Locate and identify every blood parasite.
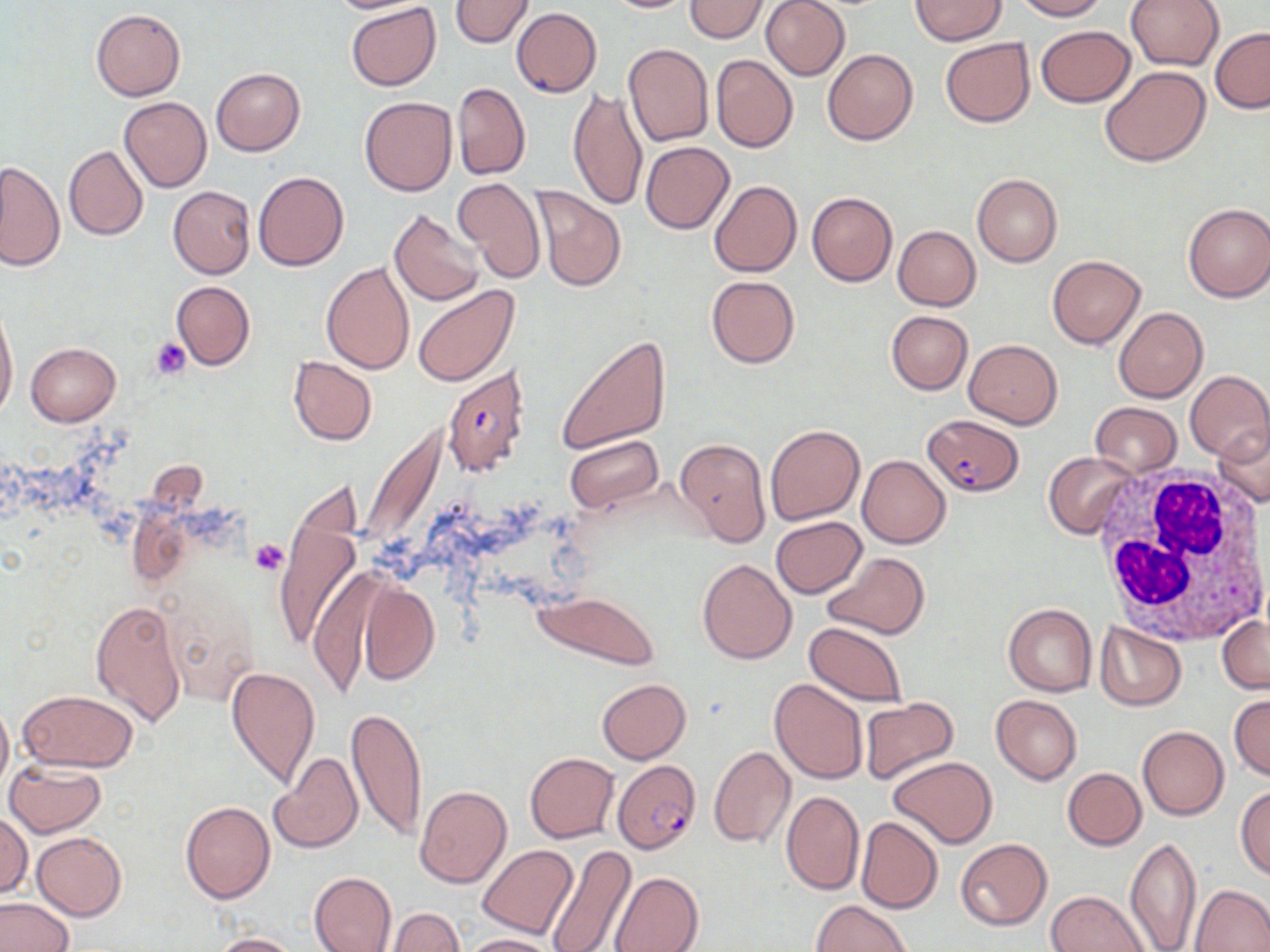

Approximate bounding boxes as [x1, y1, x2, y2] in pixels.
Plasmodium falciparum-infected red blood cells: [442, 367, 531, 476], [923, 414, 1024, 496], [613, 759, 700, 854].
No Plasmodium ovale, Plasmodium malariae, Plasmodium vivax, Babesia divergens, or Trypanosoma brucei observed.

Uninfected red blood cell locations: [324, 0, 431, 14], [449, 0, 535, 49], [603, 0, 700, 14], [687, 0, 769, 42], [760, 0, 849, 80], [910, 0, 1009, 44], [1010, 0, 1106, 21], [1124, 0, 1223, 71], [346, 3, 441, 91], [512, 7, 602, 97], [91, 9, 185, 101], [1035, 25, 1135, 107], [1210, 27, 1270, 113], [940, 38, 1034, 127], [623, 44, 713, 147], [822, 49, 917, 145], [711, 54, 797, 152], [211, 66, 305, 154], [1100, 66, 1208, 167], [452, 82, 530, 179], [568, 88, 648, 213], [118, 97, 210, 192], [359, 97, 457, 196], [640, 142, 734, 234], [64, 145, 147, 242], [0, 159, 65, 271], [253, 172, 348, 271], [971, 174, 1062, 267], [453, 178, 545, 281], [709, 178, 802, 278], [168, 185, 255, 278], [531, 186, 626, 291], [807, 192, 897, 287], [1182, 203, 1270, 302], [389, 209, 483, 307], [893, 225, 980, 311], [1047, 255, 1145, 348], [321, 262, 415, 374], [706, 275, 800, 367], [170, 280, 254, 370], [413, 284, 520, 389], [0, 304, 18, 425], [1114, 307, 1208, 402], [886, 311, 973, 394], [556, 334, 672, 455], [963, 339, 1063, 428], [26, 343, 120, 425], [287, 357, 378, 445], [1185, 370, 1270, 462], [1091, 403, 1182, 477], [358, 424, 446, 552], [765, 425, 864, 525], [1213, 425, 1269, 508], [564, 435, 664, 516], [674, 438, 771, 549], [1044, 452, 1136, 539], [856, 455, 950, 548], [276, 483, 361, 649], [771, 516, 867, 598], [822, 551, 928, 640], [696, 557, 797, 663], [309, 568, 382, 703], [358, 579, 440, 684], [532, 589, 660, 672], [164, 592, 259, 703], [90, 599, 188, 730], [1003, 603, 1097, 696], [1217, 615, 1269, 694], [1095, 621, 1185, 711], [804, 622, 907, 706], [225, 666, 321, 788], [596, 678, 691, 764], [769, 678, 869, 786], [18, 689, 139, 772], [1229, 693, 1270, 781], [990, 694, 1082, 784], [0, 695, 13, 794], [858, 696, 960, 787], [346, 707, 429, 839], [1137, 726, 1229, 820], [708, 747, 796, 850], [270, 752, 363, 854], [525, 753, 619, 842], [887, 755, 997, 848], [4, 762, 106, 837], [1063, 767, 1146, 850], [415, 785, 512, 889], [1235, 785, 1270, 880], [781, 791, 864, 895], [180, 801, 275, 904], [0, 813, 32, 897], [855, 816, 942, 914], [32, 831, 126, 921], [1125, 836, 1200, 952], [955, 838, 1052, 930], [477, 844, 577, 940], [545, 844, 638, 952], [309, 871, 397, 952], [608, 871, 704, 952], [1190, 884, 1270, 951], [1046, 890, 1150, 952], [0, 895, 72, 952], [812, 899, 912, 951], [385, 907, 465, 951], [212, 932, 306, 952], [463, 934, 562, 952]. White blood cell locations: [1088, 461, 1268, 647]. Platelet locations: [150, 338, 190, 379], [249, 538, 290, 575]. Slide-level diagnosis: Plasmodium falciparum. 1000x magnification. Image is 1270×952 pixels. May-Grünwald-Giemsa-stained preparation. Thin blood film. One field of a larger specimen. Light microscopy.